Locate platelets.
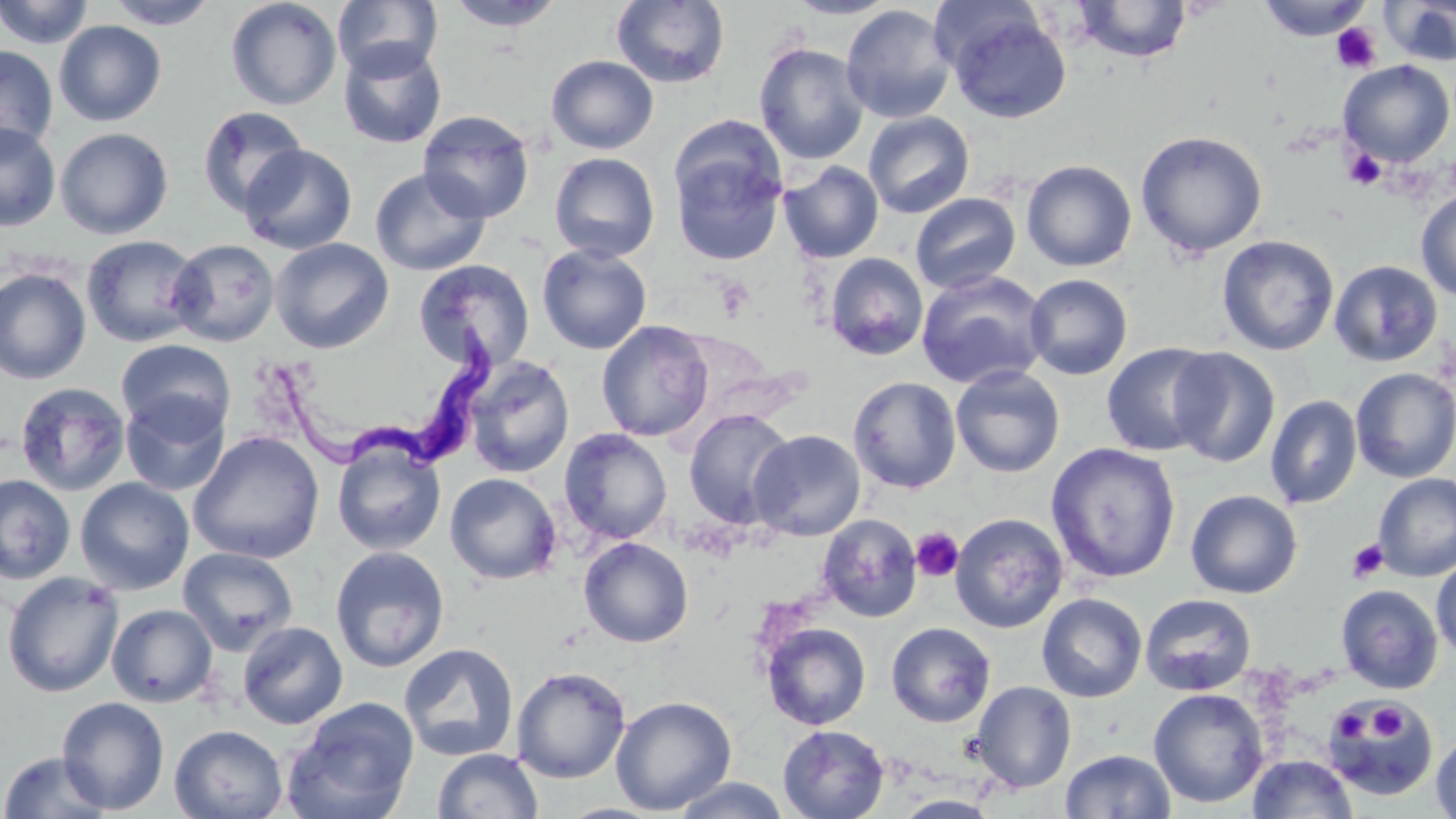

Approximate bounding boxes as named x1/y1/x2/y2 corners in pixels.
Platelets: (x1=1331, y1=23, x2=1381, y2=74), (x1=1343, y1=148, x2=1387, y2=191), (x1=911, y1=527, x2=963, y2=582), (x1=1347, y1=538, x2=1389, y2=583), (x1=1369, y1=704, x2=1408, y2=744), (x1=1330, y1=708, x2=1372, y2=745).

slide-level diagnosis = Trypanosoma brucei
stain = May-Grünwald-Giemsa
image size = 1456×819 pixels
Trypanosoma brucei locations = approximate bounding boxes as named x1/y1/x2/y2 corners in pixels: (x1=275, y1=317, x2=495, y2=478)
preparation = thin blood smear
magnification = 1000x
modality = optical microscopy
field of view = one of a larger specimen
uninfected red blood cell locations = approximate bounding boxes as named x1/y1/x2/y2 corners in pixels: (x1=0, y1=0, x2=95, y2=49), (x1=105, y1=0, x2=220, y2=29), (x1=225, y1=0, x2=342, y2=110), (x1=332, y1=0, x2=442, y2=81), (x1=783, y1=0, x2=901, y2=19), (x1=1074, y1=0, x2=1194, y2=63), (x1=1256, y1=0, x2=1374, y2=42), (x1=1381, y1=0, x2=1456, y2=66), (x1=445, y1=1, x2=568, y2=31), (x1=611, y1=1, x2=730, y2=89), (x1=840, y1=4, x2=957, y2=125), (x1=942, y1=6, x2=1072, y2=124), (x1=54, y1=20, x2=167, y2=126), (x1=338, y1=41, x2=447, y2=149), (x1=753, y1=42, x2=870, y2=165), (x1=0, y1=45, x2=58, y2=156), (x1=546, y1=55, x2=659, y2=155), (x1=1338, y1=60, x2=1455, y2=167), (x1=196, y1=106, x2=308, y2=217), (x1=418, y1=111, x2=535, y2=223), (x1=863, y1=111, x2=975, y2=219), (x1=0, y1=122, x2=61, y2=232), (x1=55, y1=128, x2=173, y2=240), (x1=66, y1=129, x2=187, y2=348), (x1=1135, y1=130, x2=1268, y2=258), (x1=239, y1=143, x2=358, y2=254), (x1=670, y1=143, x2=788, y2=266), (x1=549, y1=151, x2=660, y2=262), (x1=1021, y1=159, x2=1137, y2=272), (x1=779, y1=161, x2=884, y2=263), (x1=370, y1=167, x2=491, y2=277), (x1=1415, y1=190, x2=1456, y2=301), (x1=910, y1=193, x2=1021, y2=294), (x1=81, y1=234, x2=204, y2=348), (x1=1216, y1=234, x2=1340, y2=356), (x1=269, y1=237, x2=394, y2=354), (x1=167, y1=238, x2=280, y2=347), (x1=536, y1=243, x2=652, y2=355), (x1=825, y1=253, x2=928, y2=360), (x1=413, y1=259, x2=535, y2=373), (x1=1328, y1=259, x2=1444, y2=367), (x1=0, y1=267, x2=92, y2=385), (x1=916, y1=270, x2=1050, y2=390), (x1=1024, y1=274, x2=1133, y2=379), (x1=596, y1=320, x2=714, y2=442), (x1=116, y1=339, x2=235, y2=440), (x1=1101, y1=342, x2=1221, y2=457), (x1=1167, y1=347, x2=1280, y2=468), (x1=463, y1=356, x2=576, y2=478), (x1=950, y1=366, x2=1066, y2=478), (x1=1350, y1=368, x2=1456, y2=483), (x1=848, y1=376, x2=962, y2=493), (x1=14, y1=381, x2=131, y2=497), (x1=120, y1=391, x2=230, y2=497), (x1=1265, y1=395, x2=1362, y2=509), (x1=683, y1=409, x2=796, y2=529), (x1=559, y1=428, x2=672, y2=545), (x1=748, y1=429, x2=866, y2=541), (x1=188, y1=430, x2=325, y2=564), (x1=332, y1=439, x2=446, y2=556), (x1=1045, y1=442, x2=1182, y2=584), (x1=1372, y1=472, x2=1456, y2=582), (x1=445, y1=473, x2=562, y2=585), (x1=0, y1=474, x2=76, y2=584), (x1=75, y1=477, x2=194, y2=595), (x1=1185, y1=489, x2=1303, y2=599), (x1=817, y1=513, x2=923, y2=623), (x1=950, y1=513, x2=1069, y2=633), (x1=578, y1=536, x2=694, y2=648), (x1=178, y1=546, x2=298, y2=656), (x1=330, y1=546, x2=450, y2=672), (x1=1431, y1=557, x2=1456, y2=661), (x1=1, y1=571, x2=124, y2=698), (x1=1335, y1=584, x2=1443, y2=694), (x1=1036, y1=593, x2=1147, y2=703), (x1=1140, y1=594, x2=1256, y2=695), (x1=106, y1=603, x2=218, y2=707), (x1=238, y1=621, x2=348, y2=729), (x1=761, y1=622, x2=872, y2=730), (x1=886, y1=622, x2=996, y2=728), (x1=398, y1=642, x2=520, y2=762), (x1=511, y1=666, x2=631, y2=784), (x1=970, y1=680, x2=1076, y2=793), (x1=1148, y1=687, x2=1269, y2=809), (x1=610, y1=695, x2=738, y2=815), (x1=57, y1=697, x2=169, y2=814), (x1=282, y1=698, x2=420, y2=819), (x1=1325, y1=699, x2=1437, y2=801), (x1=169, y1=724, x2=288, y2=819), (x1=778, y1=724, x2=889, y2=818), (x1=1430, y1=731, x2=1456, y2=819), (x1=432, y1=748, x2=543, y2=819), (x1=1060, y1=748, x2=1176, y2=819), (x1=1, y1=751, x2=111, y2=818), (x1=1248, y1=754, x2=1357, y2=818), (x1=671, y1=777, x2=791, y2=818), (x1=890, y1=795, x2=1004, y2=818)